Locate every blood parasite and identify its species.
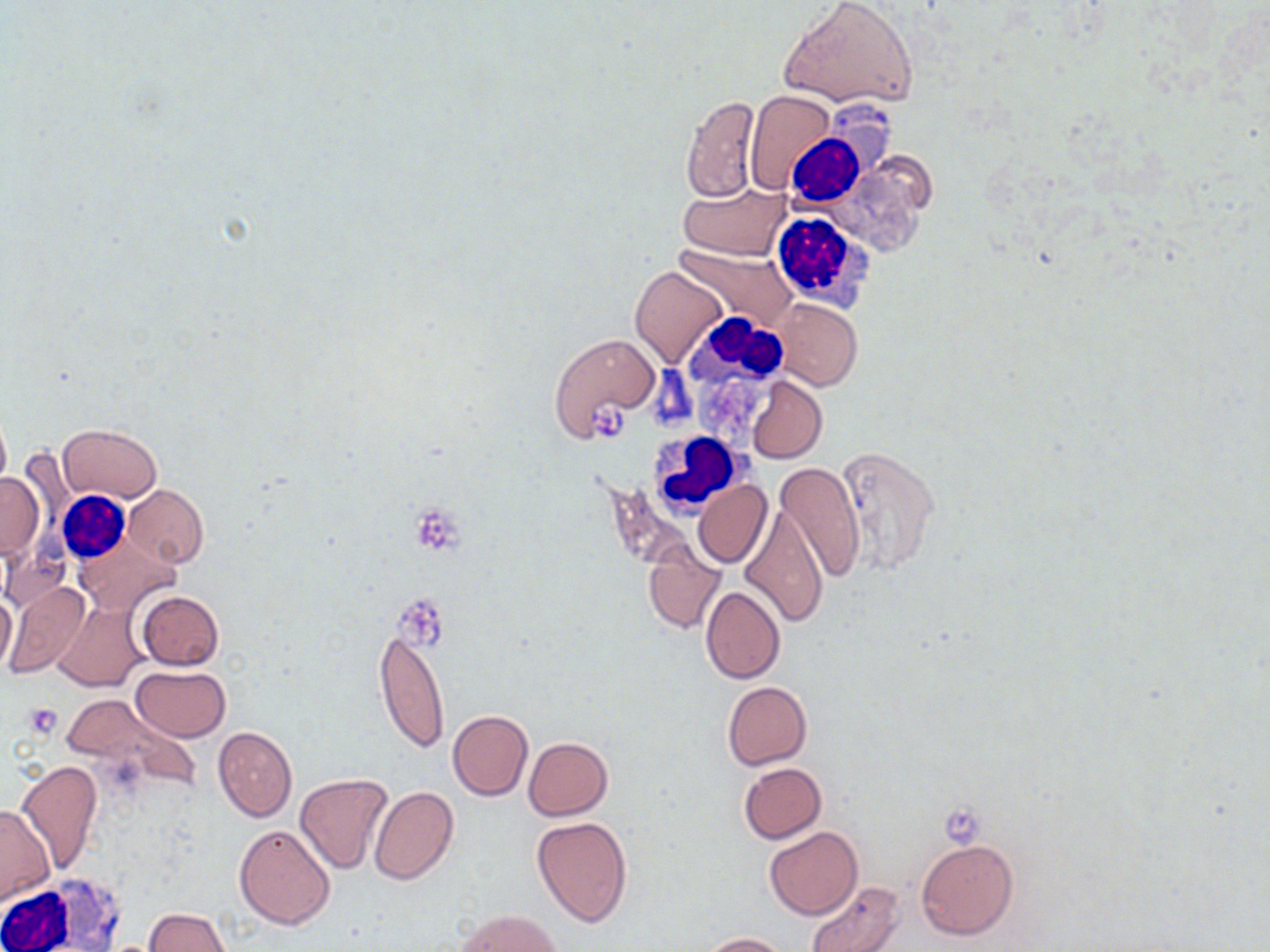
No blood parasites observed.

Approximate bounding boxes as [x1, y1, x2, y2] in pixels. Platelet locations: [590, 403, 628, 443], [410, 502, 465, 556], [393, 597, 451, 644], [22, 702, 62, 739], [940, 804, 986, 847]. Uninfected red blood cell locations: [778, 0, 920, 109], [745, 90, 834, 195], [680, 95, 761, 205], [679, 181, 790, 261], [676, 244, 796, 331], [631, 265, 725, 368], [771, 298, 862, 390], [548, 332, 661, 440], [747, 377, 827, 463], [0, 409, 11, 497], [59, 424, 160, 503], [830, 448, 941, 577], [774, 463, 865, 582], [0, 471, 43, 559], [694, 479, 771, 569], [123, 485, 208, 568], [739, 504, 828, 628], [75, 536, 180, 614], [1, 539, 69, 614], [643, 549, 724, 633], [3, 581, 91, 681], [700, 586, 786, 683], [1, 590, 17, 677], [135, 590, 224, 670], [55, 601, 149, 693], [375, 630, 449, 756], [130, 664, 232, 742], [722, 681, 812, 770], [58, 693, 182, 780], [448, 711, 533, 801], [213, 726, 297, 821], [523, 737, 613, 820], [18, 760, 104, 875], [737, 763, 827, 844], [294, 773, 394, 875], [370, 786, 459, 885], [0, 803, 56, 904], [531, 815, 632, 927], [233, 823, 336, 929], [764, 825, 862, 920], [917, 838, 1018, 939], [803, 880, 906, 952], [142, 908, 230, 951], [457, 909, 564, 951], [698, 932, 787, 951]. White blood cell locations: [783, 131, 862, 207], [770, 208, 873, 309], [684, 313, 792, 408], [648, 430, 745, 515], [56, 492, 130, 566], [1, 878, 119, 952]. Slide-level diagnosis: no evidence of blood parasites. Thin blood smear. Captured at 1000x magnification. May-Grünwald-Giemsa stain. Optical microscopy. One field of a larger specimen. Image is 1270×952 pixels.